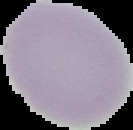

image_type: segmented cell region on a black background
image_size: 133×130 pixels
result: no malaria parasites detected
preparation: thin blood film